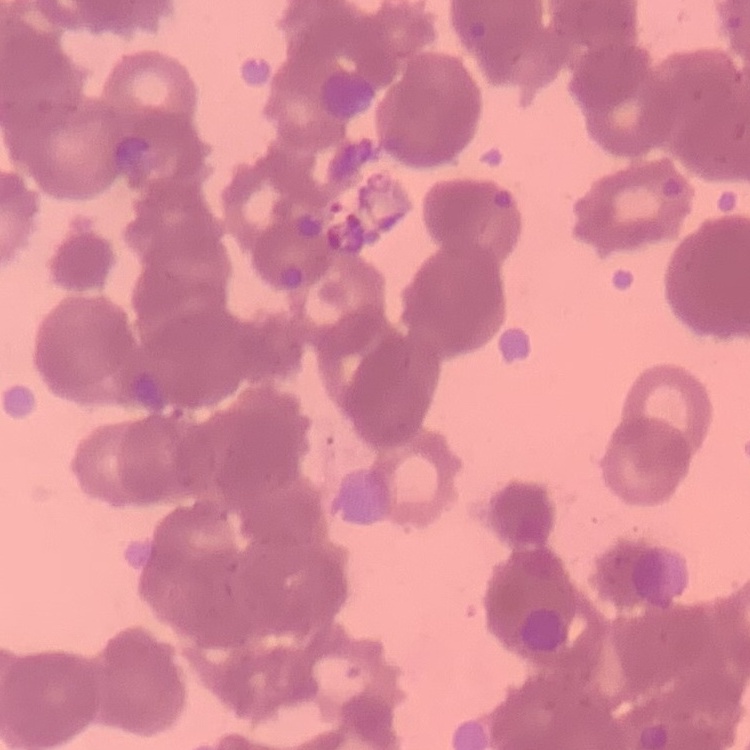

Summary:
  - Red blood cell morphology: rouleaux formation
  - Stain: Field's or Giemsa
  - Image type: one tile cut from a larger photomicrograph
  - Preparation: thin blood smear